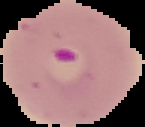 From a thin blood film. Image is 145×127 pixels. Cell region segmented out of the field of view; the surrounding area is masked to black. Malaria status: parasitized.